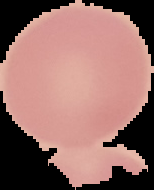
Segmented cell region on a black background. Malaria status: uninfected. From a thin blood film. Image is 154×190 pixels.